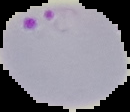

image size = 130×112 pixels
image type = segmented cell region with the area outside set to black
result = malaria parasites identified
preparation = thin blood smear